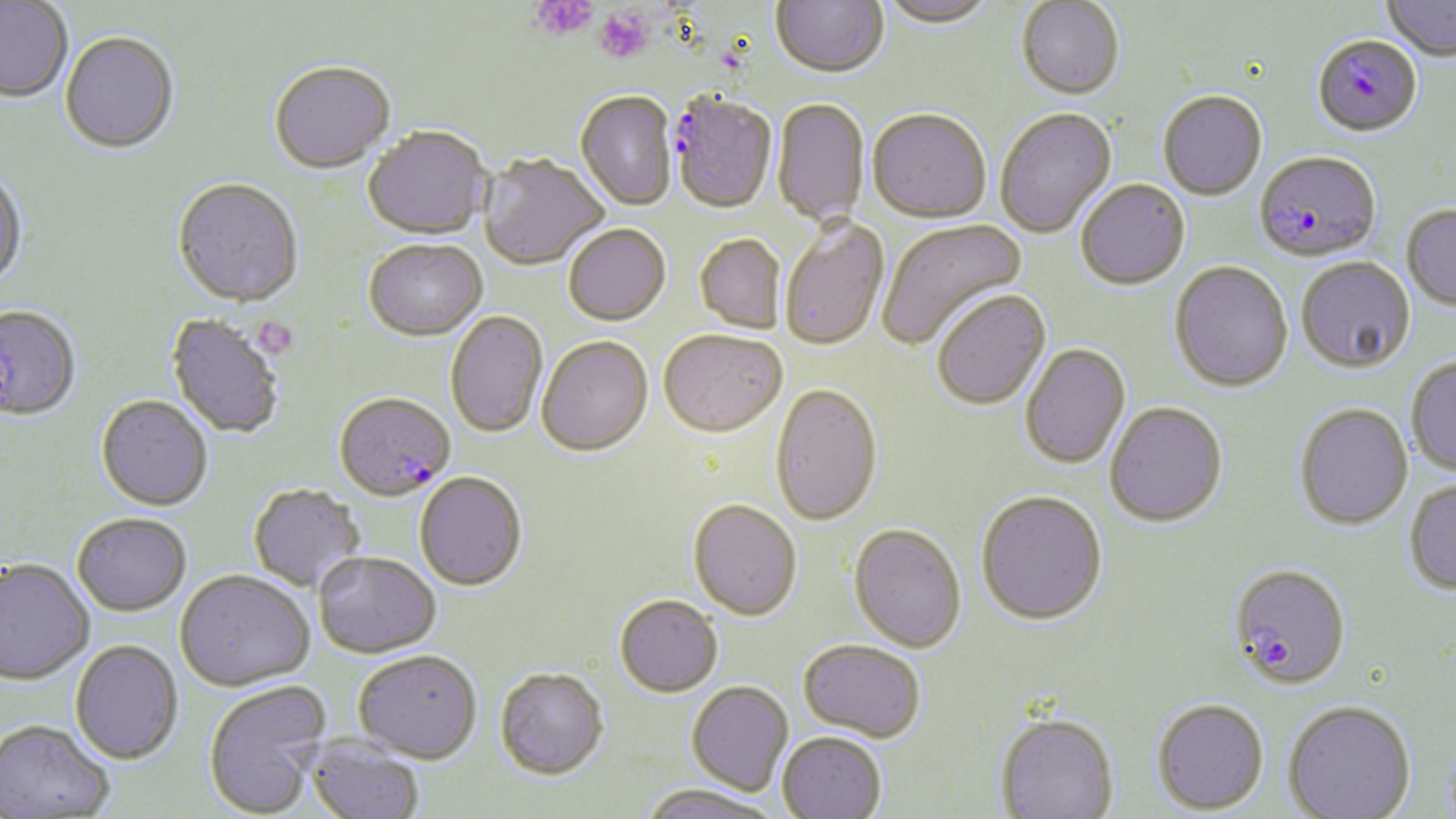
slide-level diagnosis = Plasmodium falciparum
field of view = single
uninfected red blood cell locations (subset) = approximate bounding boxes as named x1/y1/x2/y2 corners in pixels: (x1=771, y1=0, x2=888, y2=81), (x1=877, y1=0, x2=997, y2=30), (x1=1383, y1=0, x2=1456, y2=61), (x1=1016, y1=1, x2=1124, y2=102), (x1=0, y1=2, x2=73, y2=104), (x1=59, y1=33, x2=179, y2=156), (x1=269, y1=63, x2=396, y2=176), (x1=1158, y1=92, x2=1267, y2=201), (x1=575, y1=93, x2=677, y2=212), (x1=772, y1=99, x2=870, y2=229), (x1=995, y1=109, x2=1118, y2=240), (x1=868, y1=111, x2=990, y2=225), (x1=363, y1=129, x2=492, y2=242), (x1=478, y1=155, x2=609, y2=272), (x1=0, y1=167, x2=28, y2=292), (x1=172, y1=180, x2=303, y2=310), (x1=1076, y1=181, x2=1190, y2=291), (x1=1401, y1=204, x2=1456, y2=310), (x1=876, y1=218, x2=1028, y2=352), (x1=780, y1=220, x2=889, y2=353), (x1=564, y1=226, x2=671, y2=327), (x1=694, y1=235, x2=785, y2=335), (x1=364, y1=242, x2=488, y2=344), (x1=1296, y1=257, x2=1415, y2=372), (x1=1169, y1=262, x2=1294, y2=392), (x1=932, y1=291, x2=1052, y2=412), (x1=445, y1=312, x2=548, y2=438), (x1=166, y1=315, x2=285, y2=438), (x1=658, y1=332, x2=786, y2=440), (x1=536, y1=337, x2=653, y2=458), (x1=1020, y1=344, x2=1131, y2=470), (x1=1406, y1=355, x2=1456, y2=476), (x1=769, y1=384, x2=882, y2=528), (x1=95, y1=396, x2=212, y2=511), (x1=1105, y1=401, x2=1228, y2=527), (x1=1294, y1=403, x2=1413, y2=529), (x1=414, y1=473, x2=528, y2=592), (x1=1404, y1=478, x2=1456, y2=594), (x1=248, y1=483, x2=366, y2=592), (x1=976, y1=492, x2=1108, y2=627), (x1=688, y1=501, x2=802, y2=622), (x1=72, y1=512, x2=192, y2=615), (x1=848, y1=525, x2=966, y2=653), (x1=313, y1=552, x2=441, y2=658), (x1=0, y1=558, x2=94, y2=685), (x1=175, y1=570, x2=315, y2=692), (x1=614, y1=596, x2=723, y2=698), (x1=70, y1=639, x2=184, y2=764), (x1=798, y1=639, x2=926, y2=742), (x1=353, y1=651, x2=482, y2=764), (x1=495, y1=668, x2=609, y2=781), (x1=202, y1=680, x2=332, y2=817), (x1=687, y1=680, x2=793, y2=795), (x1=1151, y1=697, x2=1269, y2=814), (x1=1283, y1=699, x2=1416, y2=819), (x1=995, y1=710, x2=1119, y2=818), (x1=0, y1=719, x2=115, y2=818), (x1=777, y1=731, x2=887, y2=818), (x1=305, y1=735, x2=425, y2=819), (x1=640, y1=783, x2=780, y2=819)
Plasmodium falciparum-infected red blood cell locations (subset) = approximate bounding boxes as named x1/y1/x2/y2 corners in pixels: (x1=1313, y1=34, x2=1423, y2=137), (x1=1254, y1=151, x2=1381, y2=263), (x1=0, y1=305, x2=81, y2=421), (x1=334, y1=395, x2=455, y2=503), (x1=1229, y1=563, x2=1350, y2=689)
magnification = 1000x
preparation = thin blood smear
modality = optical microscopy
platelet locations = approximate bounding boxes as named x1/y1/x2/y2 corners in pixels: (x1=531, y1=0, x2=598, y2=42), (x1=594, y1=7, x2=654, y2=65), (x1=251, y1=315, x2=299, y2=360)
image size = 1456×819 pixels
stain = May-Grünwald-Giemsa